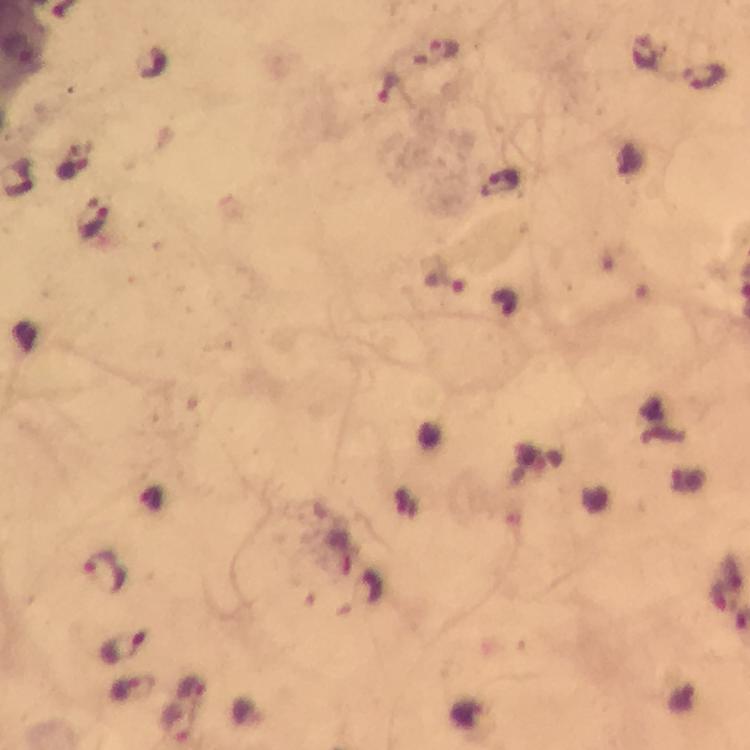 Approximate centers as {x, y} in pixels. Malaria parasite locations: {441, 51}, {648, 53}, {704, 79}, {72, 169}, {503, 184}, {92, 224}, {443, 280}, {108, 573}, {122, 647}, {176, 725}. Thick blood smear. Giemsa-stained preparation. From a malaria diagnostic workup. Image is 750×750 pixels. A crop from one field of view. Immersion oil was used. At 100x magnification. Photographed through the microscope with a smartphone camera.